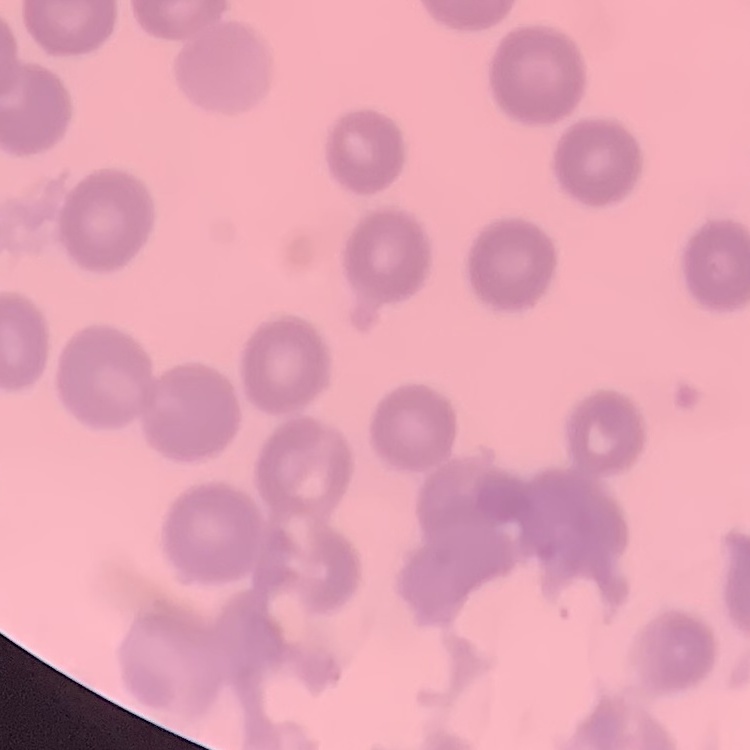

Summary:
  - Erythrocyte morphology: no rouleaux formation
  - Preparation: thin blood film
  - Image type: one tile cut from a larger photomicrograph
  - Stain: Field's or Giemsa